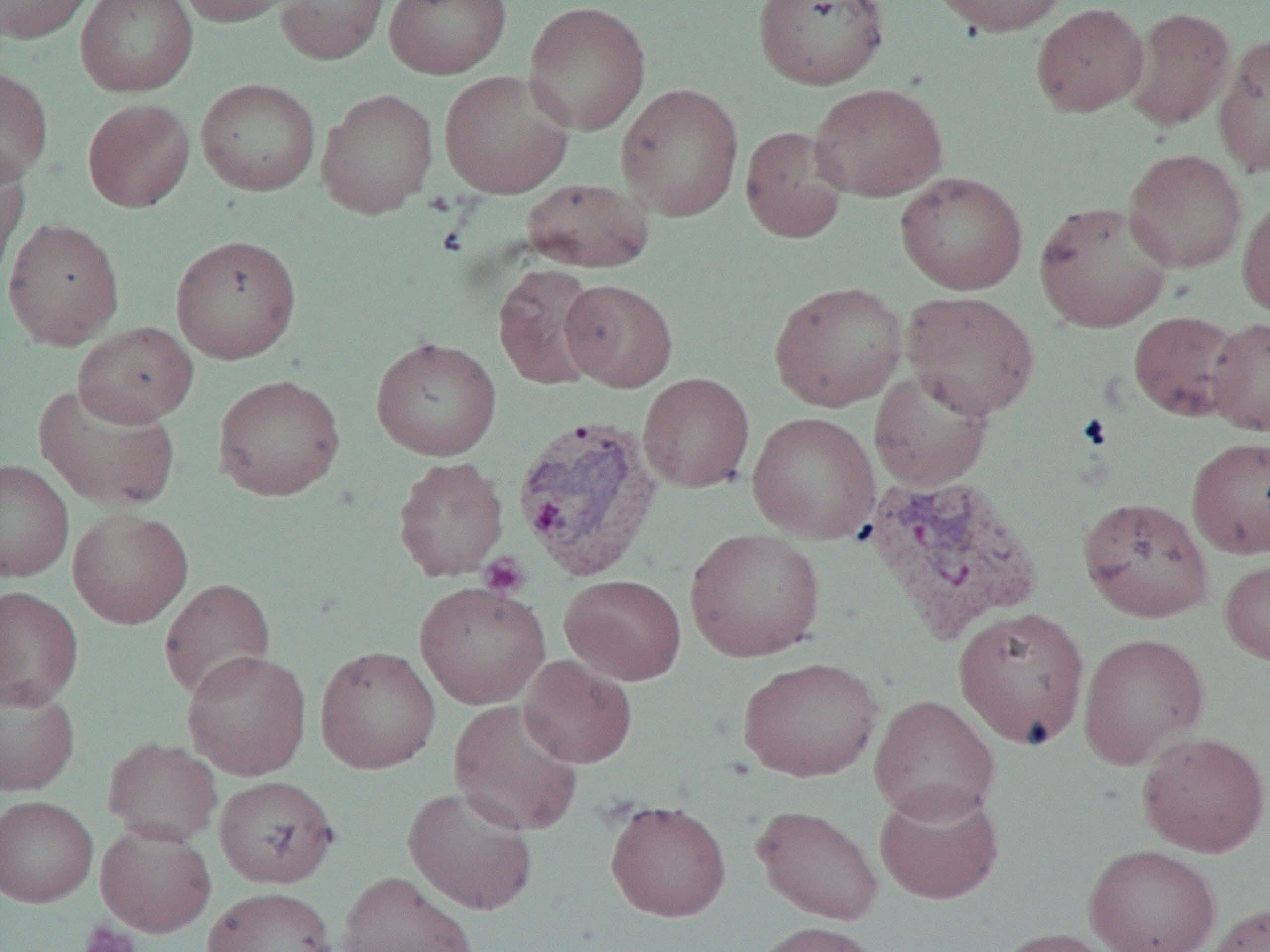

Summary:
  - Coordinate format: approximate bounding boxes as named x1/y1/x2/y2 corners in pixels
  - Plasmodium vivax-infected red blood cell locations: (x1=511, y1=414, x2=661, y2=581), (x1=863, y1=472, x2=1043, y2=642)
  - Uninfected red blood cell locations: (x1=1, y1=0, x2=94, y2=44), (x1=75, y1=0, x2=199, y2=96), (x1=177, y1=0, x2=301, y2=27), (x1=275, y1=0, x2=391, y2=65), (x1=384, y1=0, x2=510, y2=79), (x1=752, y1=0, x2=890, y2=90), (x1=931, y1=0, x2=1072, y2=37), (x1=522, y1=1, x2=651, y2=135), (x1=1031, y1=2, x2=1149, y2=117), (x1=1123, y1=6, x2=1235, y2=131), (x1=1213, y1=32, x2=1270, y2=178), (x1=0, y1=66, x2=54, y2=187), (x1=439, y1=70, x2=574, y2=198), (x1=195, y1=78, x2=320, y2=195), (x1=616, y1=82, x2=744, y2=222), (x1=809, y1=82, x2=947, y2=202), (x1=316, y1=88, x2=438, y2=218), (x1=82, y1=98, x2=195, y2=212), (x1=740, y1=125, x2=849, y2=244), (x1=0, y1=148, x2=31, y2=280), (x1=1123, y1=148, x2=1248, y2=272), (x1=895, y1=171, x2=1028, y2=295), (x1=522, y1=177, x2=654, y2=273), (x1=1236, y1=191, x2=1270, y2=318), (x1=1034, y1=200, x2=1175, y2=333), (x1=2, y1=217, x2=125, y2=348), (x1=170, y1=234, x2=302, y2=364), (x1=493, y1=264, x2=605, y2=391), (x1=559, y1=279, x2=678, y2=392), (x1=769, y1=280, x2=908, y2=412), (x1=901, y1=290, x2=1040, y2=419), (x1=1128, y1=310, x2=1246, y2=422), (x1=1206, y1=316, x2=1270, y2=436), (x1=73, y1=322, x2=198, y2=427), (x1=371, y1=336, x2=502, y2=461), (x1=869, y1=367, x2=994, y2=491), (x1=638, y1=372, x2=755, y2=493), (x1=213, y1=374, x2=345, y2=501), (x1=33, y1=382, x2=181, y2=511), (x1=747, y1=412, x2=881, y2=543), (x1=1187, y1=436, x2=1270, y2=559), (x1=392, y1=456, x2=509, y2=581), (x1=0, y1=459, x2=73, y2=582), (x1=1078, y1=496, x2=1214, y2=622), (x1=67, y1=507, x2=192, y2=629), (x1=685, y1=528, x2=825, y2=662), (x1=1220, y1=556, x2=1270, y2=666), (x1=559, y1=574, x2=687, y2=686), (x1=159, y1=577, x2=276, y2=702), (x1=414, y1=580, x2=550, y2=710), (x1=0, y1=586, x2=84, y2=710), (x1=953, y1=607, x2=1090, y2=749), (x1=1078, y1=632, x2=1210, y2=770), (x1=315, y1=645, x2=441, y2=774), (x1=182, y1=650, x2=312, y2=780), (x1=519, y1=655, x2=637, y2=768), (x1=738, y1=657, x2=883, y2=782), (x1=0, y1=679, x2=80, y2=796), (x1=869, y1=694, x2=1001, y2=823), (x1=448, y1=699, x2=584, y2=836), (x1=1136, y1=731, x2=1270, y2=857), (x1=103, y1=736, x2=222, y2=846), (x1=214, y1=775, x2=339, y2=888), (x1=874, y1=783, x2=1004, y2=904), (x1=403, y1=785, x2=539, y2=916), (x1=0, y1=795, x2=98, y2=907), (x1=605, y1=798, x2=732, y2=922), (x1=751, y1=804, x2=884, y2=925), (x1=95, y1=822, x2=217, y2=937), (x1=1083, y1=844, x2=1221, y2=952), (x1=338, y1=870, x2=479, y2=952), (x1=202, y1=887, x2=337, y2=952), (x1=1202, y1=901, x2=1270, y2=952), (x1=751, y1=921, x2=882, y2=952), (x1=988, y1=926, x2=1122, y2=952)
  - Platelet locations: (x1=480, y1=554, x2=530, y2=599), (x1=78, y1=920, x2=140, y2=952)
  - Slide-level diagnosis: Plasmodium vivax
  - Modality: optical microscopy
  - Field of view: one of a larger specimen
  - Image size: 1270×952 pixels
  - Magnification: 1000x
  - Preparation: thin blood smear